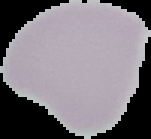
image_size: 151×139 pixels
preparation: thin blood smear
image_type: segmented cell region with the area outside set to black
result: no Plasmodium parasites detected